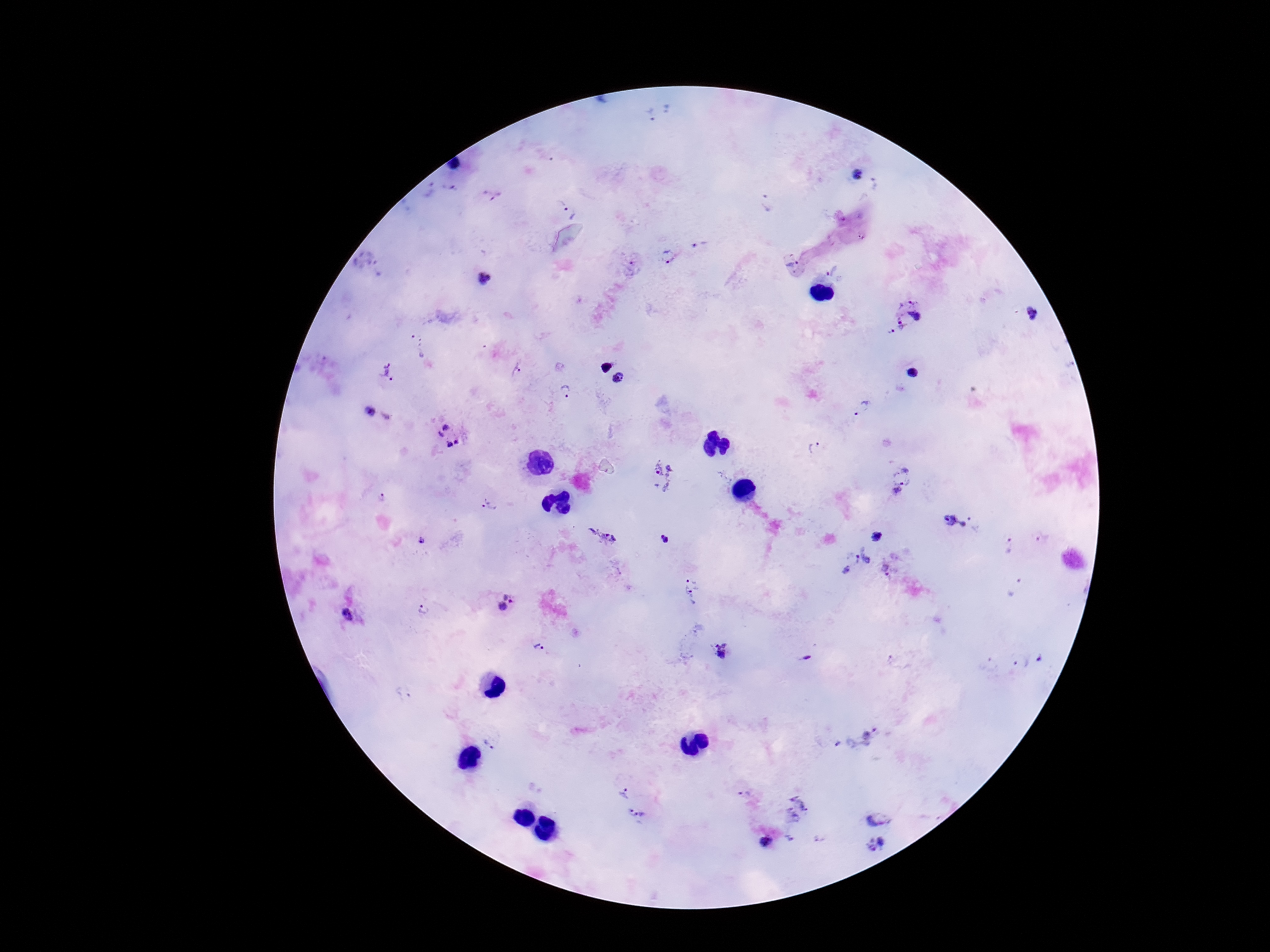

Approximate centers as [x, y] in pixels.
Summary:
  - Plasmodium parasite locations: [652, 114], [857, 176], [452, 188], [429, 191], [492, 195], [768, 203], [568, 210], [863, 235], [701, 246], [668, 255], [792, 261], [632, 268], [832, 272], [485, 279], [1034, 314], [899, 315], [604, 366], [516, 370], [388, 373], [911, 373], [618, 379], [567, 392], [860, 407], [373, 411], [449, 435], [815, 448], [661, 476], [901, 483], [381, 498], [488, 506], [956, 521], [877, 536], [602, 537], [1043, 538], [665, 540], [1010, 547], [854, 561], [887, 568], [1015, 588], [693, 591], [505, 602], [425, 609], [349, 613], [541, 645], [724, 653], [1042, 659], [1019, 661], [405, 692], [858, 736], [491, 742], [624, 792], [799, 810], [880, 815], [638, 816], [767, 843], [877, 847]
  - Preparation: thick peripheral-blood smear
  - Field of view: one from this slide
  - Magnification: 100x
  - Capture: smartphone camera through the microscope eyepiece
  - Image size: 1270×952 pixels
  - Patient malaria status: infected
  - Stain: Giemsa